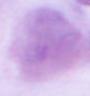
identification = red blood cell
modality = micrograph
magnification = 1000x